Comment on the morphology of the erythrocytes.
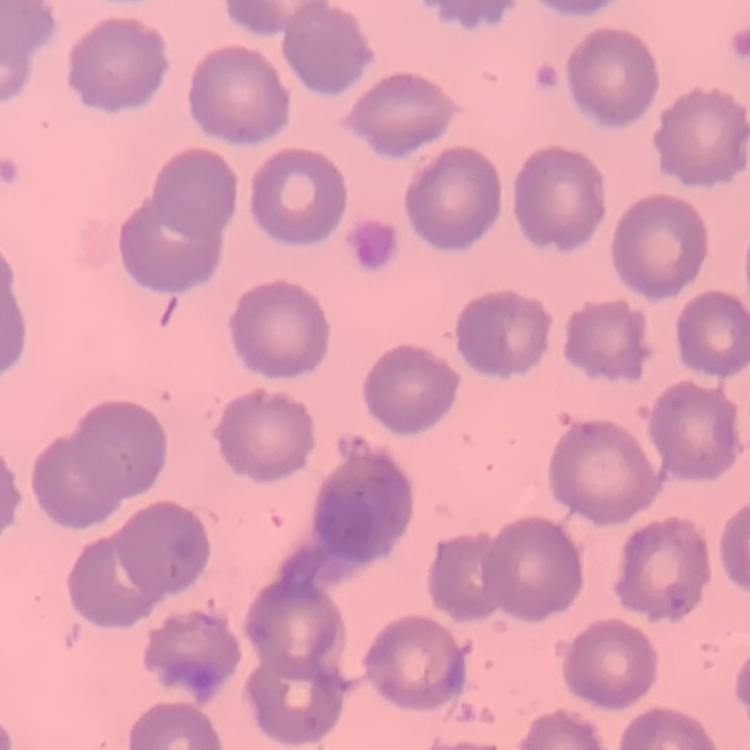
No rouleaux formation.

One tile cut from a larger photomicrograph. Thin blood film. Field's or Giemsa stain.